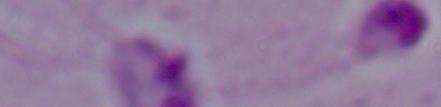
Summary:
  - Identification: Leishmania
  - Magnification: 1000x
  - Modality: micrograph